Outline each blood parasite and name the species.
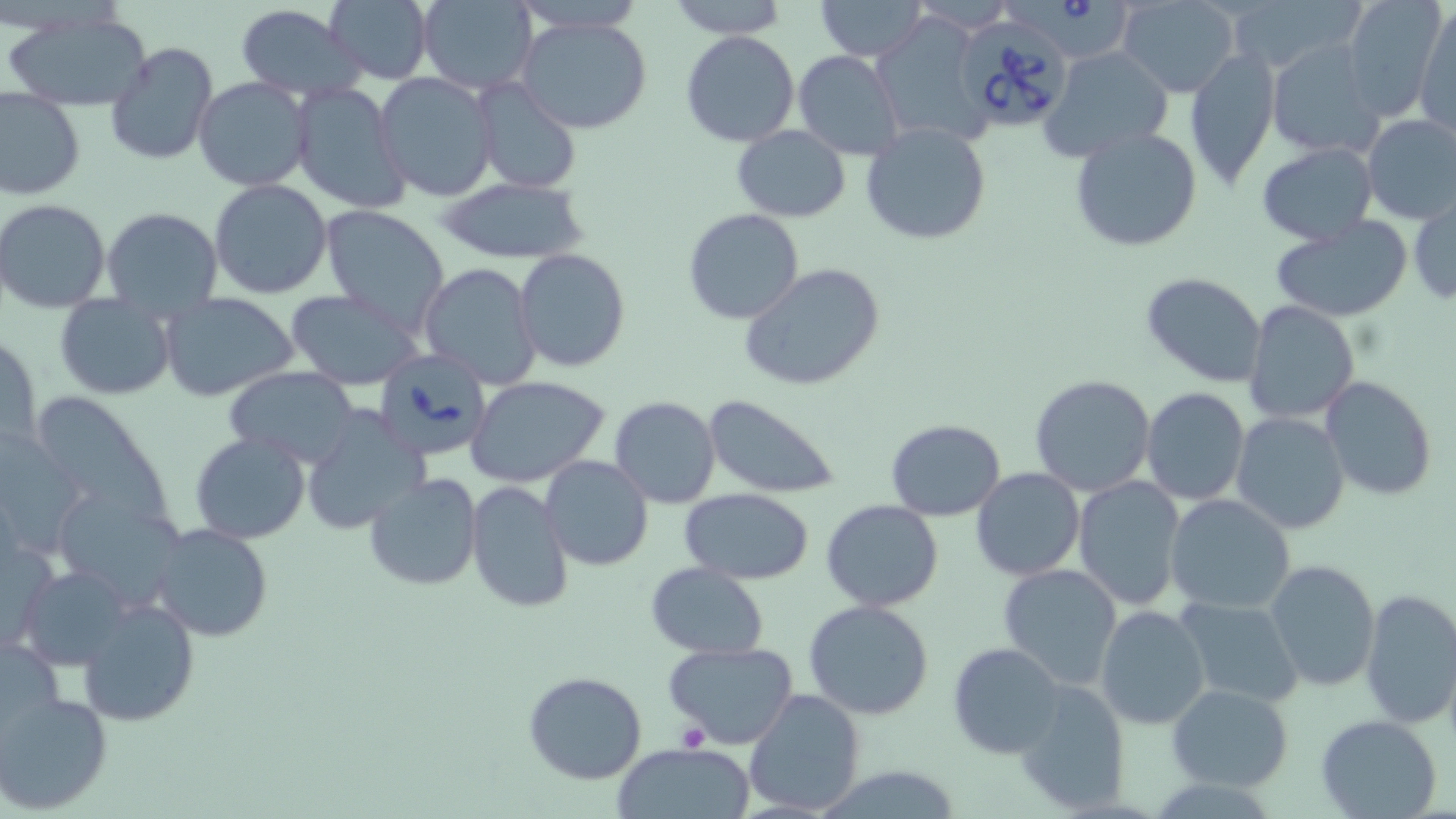
Approximate bounding boxes as [x1, y1, x2, y2] in pixels.
Babesia divergens-infected red blood cells: [999, 0, 1133, 58], [951, 12, 1073, 132], [370, 347, 494, 462].
No Plasmodium falciparum, Plasmodium ovale, Plasmodium malariae, Plasmodium vivax, or Trypanosoma brucei observed.

Summary:
  - Uninfected red blood cell locations: [324, 0, 433, 83], [416, 0, 539, 94], [513, 0, 647, 34], [667, 0, 787, 39], [1119, 0, 1241, 97], [1228, 0, 1363, 77], [1341, 0, 1447, 119], [815, 1, 929, 60], [234, 3, 365, 99], [1414, 4, 1456, 135], [3, 13, 156, 110], [869, 14, 992, 151], [514, 16, 656, 136], [680, 30, 800, 146], [104, 41, 217, 167], [1267, 41, 1383, 159], [1039, 46, 1175, 164], [1184, 48, 1281, 191], [794, 49, 906, 161], [374, 73, 499, 202], [193, 76, 313, 192], [472, 80, 582, 197], [289, 81, 411, 215], [0, 88, 85, 200], [1360, 114, 1456, 225], [863, 121, 990, 245], [732, 124, 851, 223], [1068, 125, 1206, 252], [1255, 142, 1379, 246], [434, 177, 590, 264], [208, 180, 334, 300], [1408, 192, 1455, 306], [1, 199, 114, 314], [319, 204, 451, 334], [100, 207, 224, 315], [683, 208, 804, 324], [1267, 217, 1415, 322], [514, 248, 630, 371], [418, 262, 543, 387], [740, 264, 887, 391], [1141, 272, 1269, 388], [284, 288, 424, 390], [159, 292, 299, 403], [54, 295, 175, 401], [1243, 300, 1360, 425], [1, 331, 42, 458], [225, 366, 362, 468], [1029, 374, 1157, 497], [466, 375, 612, 491], [1320, 375, 1438, 501], [1140, 387, 1251, 507], [26, 391, 171, 525], [702, 394, 845, 499], [609, 395, 722, 509], [301, 406, 429, 535], [1231, 412, 1350, 535], [884, 419, 1006, 521], [0, 431, 92, 560], [189, 433, 311, 544], [539, 455, 653, 571], [971, 469, 1086, 581], [365, 473, 483, 591], [1073, 476, 1186, 612], [465, 480, 573, 613], [50, 486, 190, 606], [680, 487, 814, 585], [1164, 493, 1296, 614], [822, 500, 944, 612], [151, 523, 273, 642], [1, 525, 56, 652], [1263, 559, 1380, 691], [646, 562, 769, 659], [20, 563, 132, 670], [997, 563, 1124, 688], [1357, 588, 1456, 731], [1174, 595, 1305, 708], [76, 596, 200, 727], [802, 601, 934, 720], [1096, 604, 1211, 731], [1, 632, 67, 744], [664, 641, 800, 750], [948, 641, 1067, 759], [523, 672, 647, 785], [1013, 679, 1130, 812], [1167, 684, 1293, 791], [743, 688, 867, 816], [0, 689, 114, 814], [1314, 714, 1443, 819], [613, 741, 755, 819]
  - Platelet locations: [675, 724, 709, 751]
  - Slide-level diagnosis: Babesia divergens
  - Field of view: one of a larger specimen
  - Preparation: thin blood smear
  - Stain: May-Grünwald-Giemsa
  - Image size: 1456×819 pixels
  - Magnification: 1000x
  - Modality: optical microscopy